State which parasite is depicted.
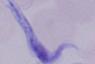
This is a trypanosome.

Captured at 1000x magnification. Micrograph.